Locate every blood parasite and identify its species.
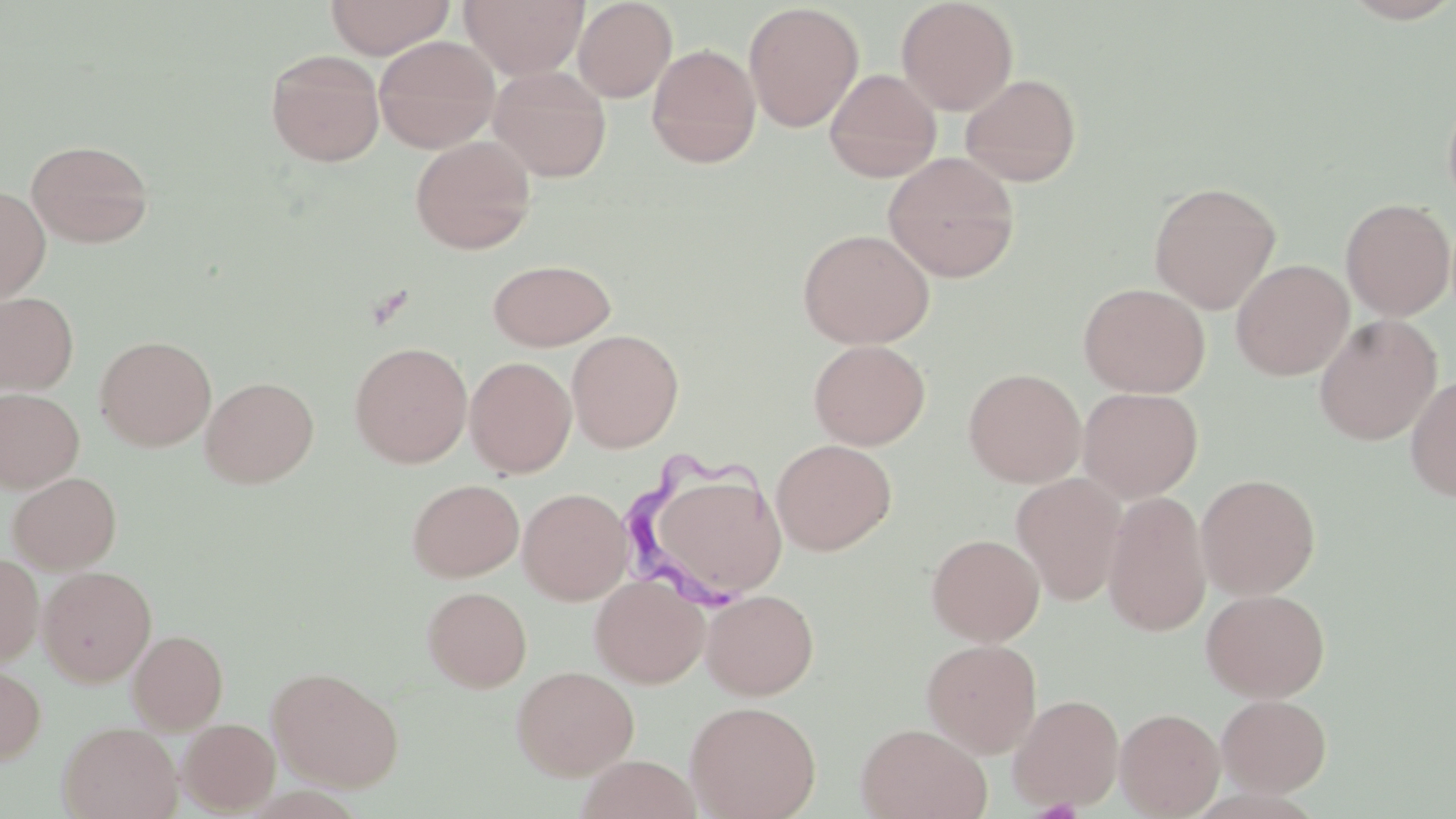

Approximate bounding boxes as [x1, y1, x2, y2] in pixels.
Trypanosoma brucei: [621, 446, 778, 616].
No Plasmodium falciparum, Plasmodium ovale, Plasmodium malariae, Plasmodium vivax, or Babesia divergens observed.

slide-level diagnosis = Trypanosoma brucei
uninfected red blood cell locations = approximate bounding boxes as [x1, y1, x2, y2] in pixels: [324, 0, 455, 58], [459, 0, 588, 79], [573, 0, 677, 102], [896, 0, 1019, 115], [1340, 0, 1456, 24], [743, 3, 864, 132], [374, 35, 500, 154], [646, 43, 761, 168], [265, 49, 385, 166], [488, 65, 611, 181], [824, 68, 942, 182], [960, 73, 1082, 187], [1442, 83, 1456, 217], [410, 135, 536, 254], [25, 138, 155, 248], [883, 152, 1020, 282], [1148, 181, 1282, 314], [0, 186, 51, 303], [1340, 197, 1455, 321], [798, 228, 935, 348], [488, 259, 616, 350], [1231, 259, 1353, 380], [1078, 282, 1211, 398], [0, 291, 78, 395], [1314, 314, 1442, 446], [567, 329, 684, 453], [95, 335, 216, 451], [808, 339, 930, 449], [350, 341, 472, 467], [465, 356, 576, 478], [964, 368, 1086, 487], [1405, 373, 1456, 502], [200, 376, 319, 488], [0, 387, 84, 492], [1079, 387, 1203, 502], [771, 439, 896, 555], [7, 471, 122, 573], [1011, 473, 1127, 606], [1196, 473, 1320, 599], [407, 478, 524, 581], [518, 488, 632, 604], [662, 490, 796, 586], [1102, 490, 1212, 638], [926, 533, 1044, 645], [0, 553, 44, 666], [38, 566, 157, 686], [590, 574, 708, 688], [422, 586, 532, 692], [702, 588, 819, 699], [1201, 588, 1330, 702], [128, 629, 228, 733], [921, 638, 1042, 757], [0, 663, 45, 765], [511, 665, 639, 780], [266, 666, 404, 792], [1008, 693, 1124, 812], [1216, 694, 1331, 796], [685, 700, 821, 819], [1115, 707, 1224, 818], [178, 718, 280, 813], [58, 721, 182, 819], [855, 723, 992, 819], [574, 757, 704, 819]
magnification = 1000x
preparation = thin blood film
image size = 1456×819 pixels
field of view = single
stain = May-Grünwald-Giemsa
modality = light microscopy